Identify the parasite.
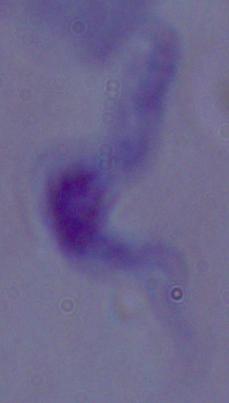

A trypanosome.

Summary:
  - Magnification: 1000x
  - Modality: photomicrograph